State which parasite is depicted.
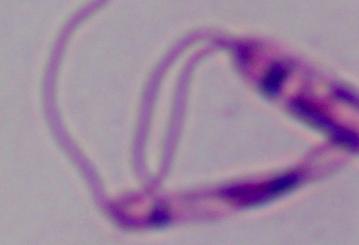

Leishmania.

Summary:
  - Magnification: 1000x
  - Modality: photomicrograph